Classify this cell by malaria status.
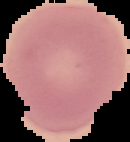
It is uninfected.

Summary:
  - Image size: 130×142 pixels
  - Preparation: thin blood film
  - Image type: segmented cell region with the area outside set to black